State the blood parasite species.
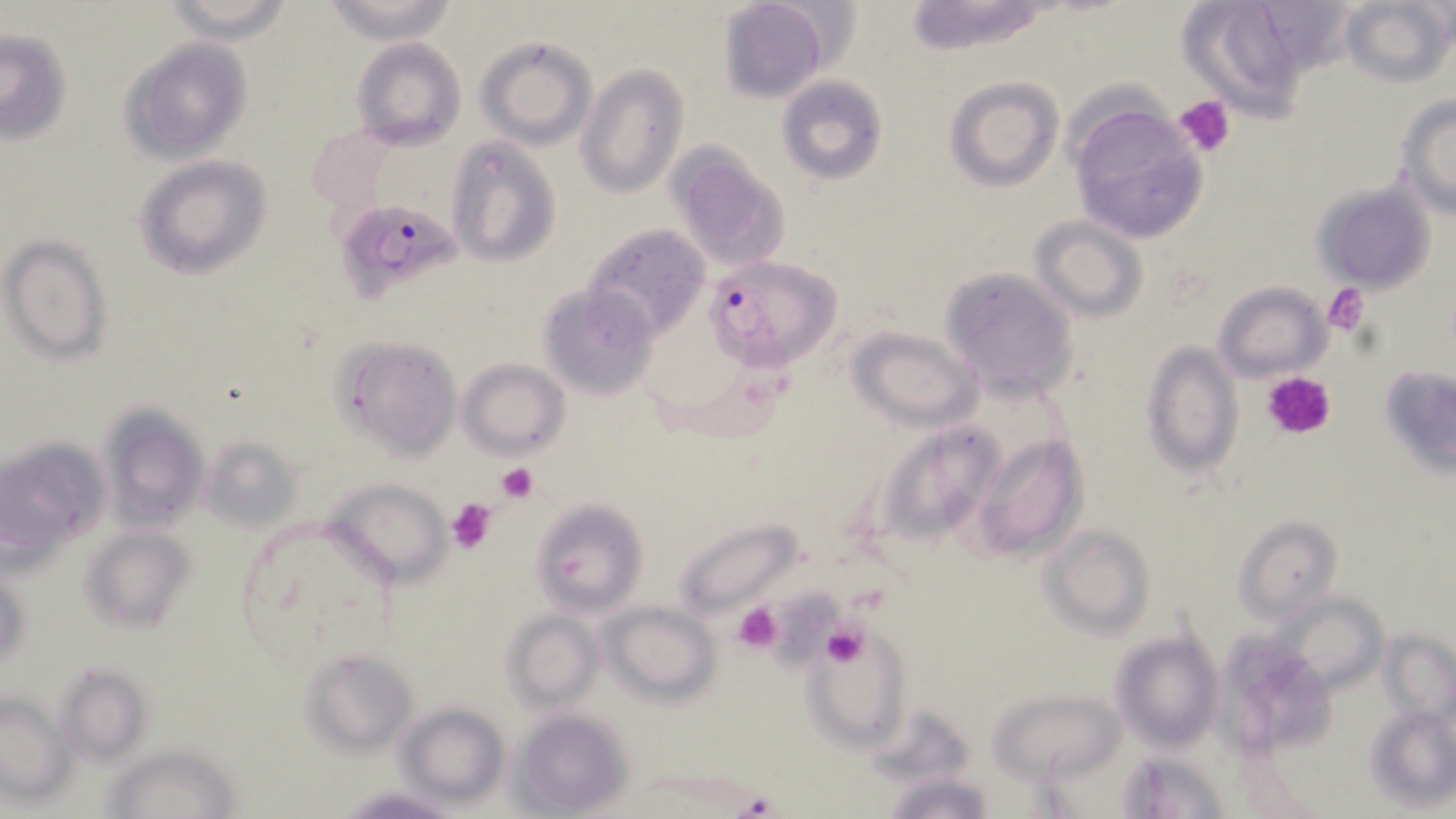
Plasmodium falciparum.

Summary:
  - Coordinate format: approximate bounding boxes as named x1/y1/x2/y2 corners in pixels
  - Uninfected red blood cell locations: (x1=162, y1=0, x2=293, y2=42), (x1=318, y1=0, x2=461, y2=44), (x1=717, y1=0, x2=832, y2=102), (x1=1176, y1=0, x2=1325, y2=121), (x1=1338, y1=0, x2=1452, y2=89), (x1=896, y1=1, x2=1062, y2=54), (x1=0, y1=28, x2=73, y2=144), (x1=474, y1=34, x2=597, y2=149), (x1=351, y1=37, x2=466, y2=152), (x1=121, y1=39, x2=252, y2=163), (x1=576, y1=63, x2=686, y2=199), (x1=775, y1=75, x2=888, y2=185), (x1=943, y1=76, x2=1064, y2=193), (x1=1394, y1=94, x2=1456, y2=218), (x1=1067, y1=96, x2=1211, y2=243), (x1=446, y1=138, x2=561, y2=268), (x1=666, y1=146, x2=794, y2=273), (x1=134, y1=157, x2=273, y2=280), (x1=1310, y1=180, x2=1437, y2=292), (x1=1029, y1=216, x2=1149, y2=324), (x1=581, y1=223, x2=714, y2=344), (x1=2, y1=236, x2=113, y2=363), (x1=938, y1=267, x2=1080, y2=402), (x1=1211, y1=281, x2=1331, y2=383), (x1=538, y1=285, x2=660, y2=402), (x1=846, y1=326, x2=983, y2=430), (x1=330, y1=336, x2=461, y2=460), (x1=1140, y1=342, x2=1244, y2=478), (x1=457, y1=358, x2=571, y2=458), (x1=1380, y1=363, x2=1456, y2=472), (x1=99, y1=403, x2=208, y2=530), (x1=869, y1=416, x2=1010, y2=555), (x1=971, y1=432, x2=1087, y2=562), (x1=200, y1=433, x2=305, y2=534), (x1=1, y1=434, x2=107, y2=560), (x1=322, y1=475, x2=452, y2=588), (x1=530, y1=498, x2=648, y2=616), (x1=1233, y1=515, x2=1342, y2=626), (x1=673, y1=517, x2=803, y2=625), (x1=1040, y1=524, x2=1156, y2=639), (x1=80, y1=525, x2=193, y2=634), (x1=1, y1=569, x2=32, y2=668), (x1=1274, y1=592, x2=1389, y2=693), (x1=604, y1=600, x2=720, y2=704), (x1=503, y1=610, x2=604, y2=710), (x1=806, y1=625, x2=912, y2=750), (x1=1379, y1=630, x2=1456, y2=727), (x1=1110, y1=631, x2=1225, y2=754), (x1=1215, y1=634, x2=1338, y2=761), (x1=300, y1=649, x2=420, y2=756), (x1=54, y1=662, x2=151, y2=763), (x1=989, y1=688, x2=1125, y2=784), (x1=0, y1=694, x2=73, y2=800), (x1=396, y1=703, x2=510, y2=809), (x1=512, y1=707, x2=635, y2=816), (x1=1363, y1=707, x2=1456, y2=810), (x1=104, y1=744, x2=242, y2=819), (x1=1115, y1=750, x2=1232, y2=819), (x1=882, y1=772, x2=996, y2=819), (x1=337, y1=786, x2=462, y2=818)
  - Plasmodium falciparum-infected red blood cell locations: (x1=347, y1=201, x2=467, y2=303), (x1=705, y1=254, x2=844, y2=373)
  - Platelet locations: (x1=1174, y1=94, x2=1236, y2=158), (x1=1324, y1=283, x2=1371, y2=336), (x1=1264, y1=373, x2=1337, y2=440), (x1=496, y1=462, x2=537, y2=503), (x1=445, y1=496, x2=499, y2=553), (x1=730, y1=601, x2=785, y2=653), (x1=821, y1=623, x2=868, y2=668), (x1=735, y1=791, x2=780, y2=817)
  - Field of view: single
  - Stain: May-Grünwald-Giemsa
  - Preparation: thin blood film
  - Magnification: 1000x
  - Modality: optical microscopy
  - Image size: 1456×819 pixels